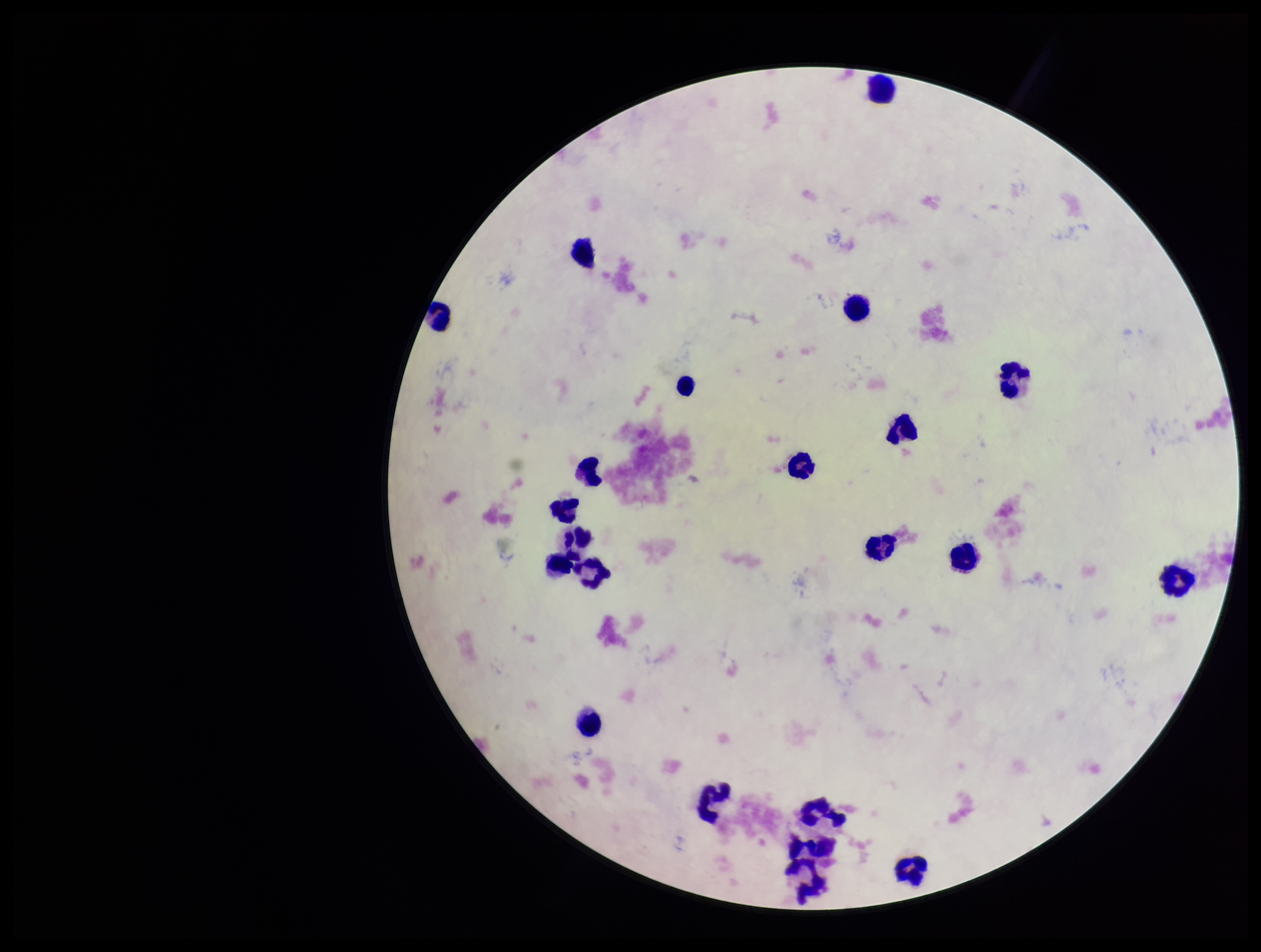

Parasite count: 0. Patient malaria status: negative. Image is 1261×952 pixels. Leukocyte count: 21. Plasmodium parasites: none identified. Preparation: thick smear. Smartphone photograph taken through the eyepiece of a microscope. Single field of view. Stained with Giemsa.